Describe the morphology of the red blood cells.
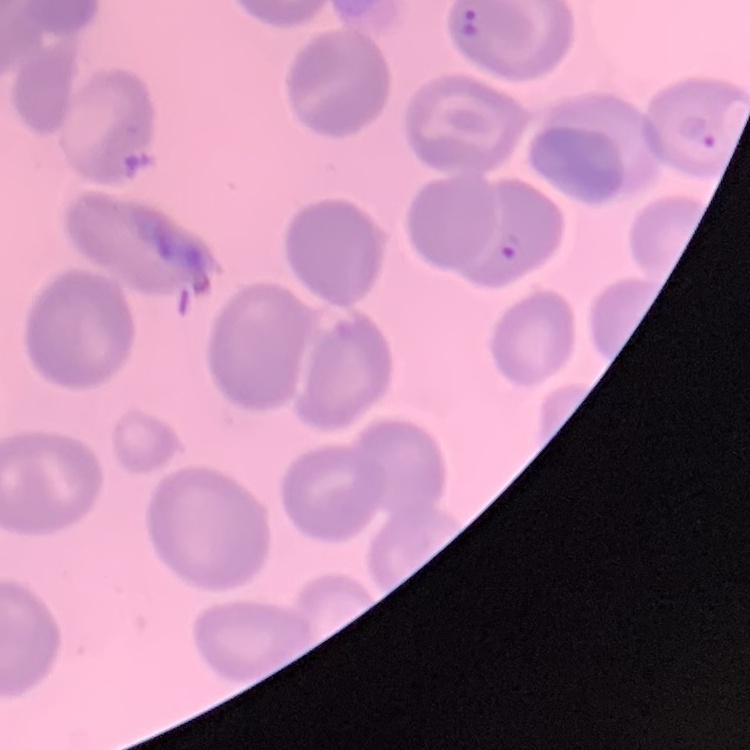

No rouleaux formation.

One tile cut from a larger photomicrograph. Thin peripheral smear. Field's or Giemsa stain.